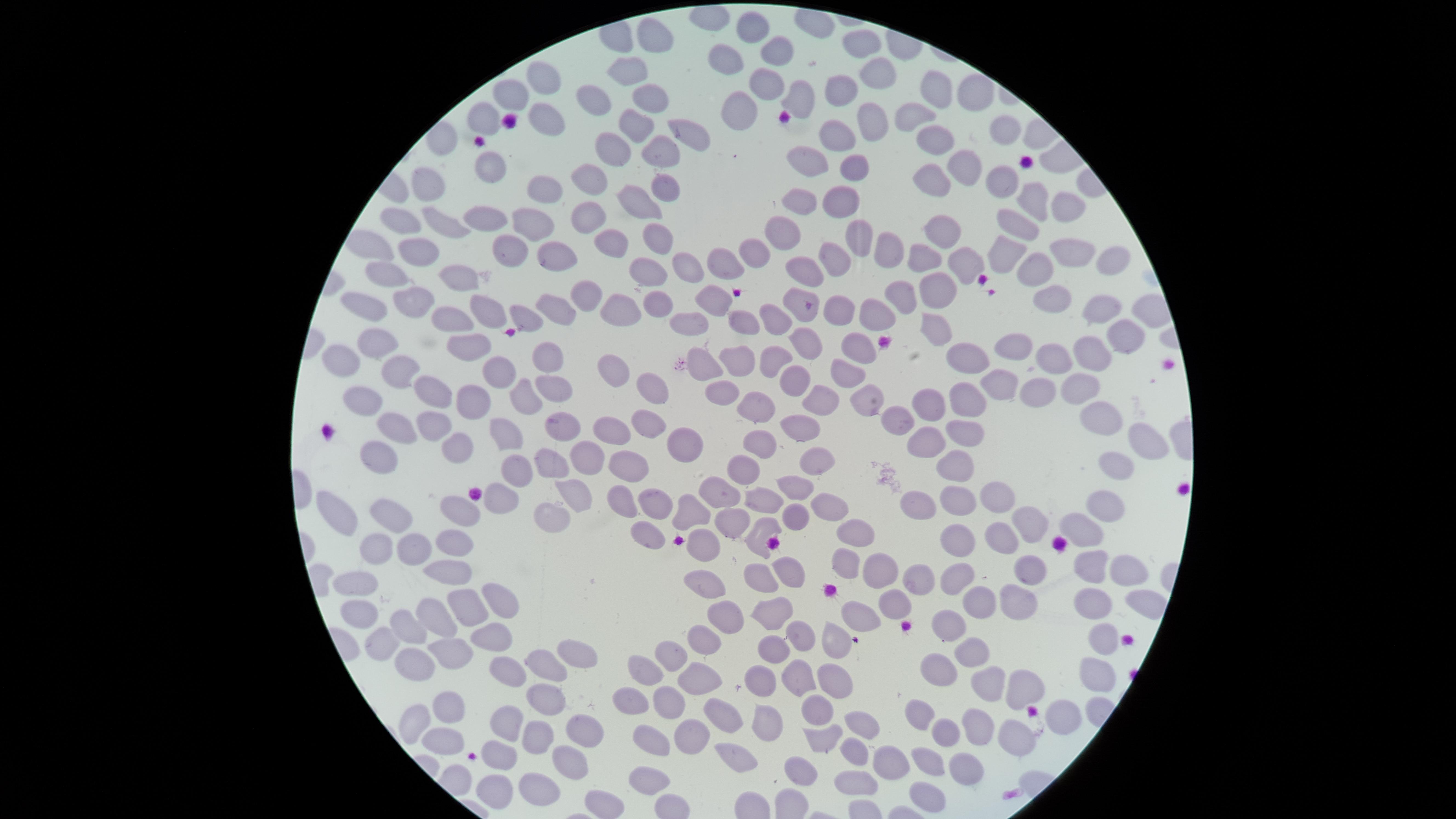

{
  "presence": "no malaria parasites detected",
  "preparation": "thin blood smear",
  "image_size": "1456×819 pixels",
  "capture": "smartphone photograph through the microscope eyepiece",
  "visible_region": "circular",
  "stain": "Giemsa",
  "field_of_view": "single",
  "uninfected_red_blood_cells": "approximate marker points as (x, y) in pixels: (753, 28), (651, 37), (862, 42), (770, 50), (722, 57), (632, 66), (875, 74), (543, 75), (764, 85), (834, 88), (511, 90), (937, 90), (971, 91), (647, 93), (591, 96), (799, 96), (737, 110), (914, 112), (485, 114), (547, 115), (872, 122), (631, 124), (688, 128), (1001, 130), (833, 136), (930, 136), (664, 152), (614, 154), (970, 161), (805, 162), (854, 165), (488, 166), (587, 172), (930, 177), (1003, 178), (430, 179), (540, 188), (659, 195), (803, 195), (1029, 197), (839, 198), (1065, 206), (635, 211), (485, 217), (587, 217), (401, 221), (531, 222), (446, 225), (1016, 225), (783, 226), (855, 237), (942, 237), (615, 239), (651, 239), (374, 241), (885, 246), (758, 247), (414, 249), (512, 249), (1072, 249), (1001, 251), (833, 255), (925, 257), (719, 259), (956, 260), (1108, 261), (555, 263), (686, 265), (648, 267), (808, 269), (389, 271), (1030, 271), (456, 273), (936, 283), (589, 290), (900, 294), (793, 297), (716, 298), (406, 300), (656, 303), (1052, 303), (366, 307), (838, 308), (551, 309), (620, 310), (1104, 310), (485, 314), (776, 314), (871, 314), (524, 316), (447, 320), (689, 320), (742, 320), (935, 324), (1127, 338), (374, 340), (808, 344), (1012, 346), (460, 347), (857, 351), (543, 352), (1089, 352), (968, 354), (1049, 354), (339, 356), (779, 356), (734, 359), (394, 362), (498, 368), (706, 368), (614, 371), (841, 375), (999, 381), (793, 382), (1076, 383), (549, 384), (435, 388), (1044, 388), (721, 389), (648, 391), (525, 392), (966, 398), (358, 400), (470, 402), (822, 402), (870, 402), (926, 402), (753, 406), (1096, 410), (430, 416), (897, 418), (648, 420), (391, 423), (561, 423), (801, 426), (502, 427), (606, 428), (969, 432), (685, 440), (928, 440), (758, 442), (452, 444), (1145, 447), (377, 455), (584, 456), (817, 460), (548, 465), (954, 465), (1115, 465), (622, 466), (516, 467), (746, 467), (796, 486), (719, 489), (574, 490), (999, 494), (767, 496), (621, 498), (496, 502), (917, 502), (652, 504), (948, 504), (823, 506), (1104, 509), (334, 511), (394, 511), (458, 512), (791, 515), (549, 516), (689, 517), (730, 522), (1033, 522), (1078, 524), (851, 531), (647, 532), (757, 534), (999, 535), (460, 538), (966, 538), (707, 545), (403, 547), (366, 548), (842, 559), (1086, 566), (451, 567), (787, 567), (1128, 571), (876, 572), (1024, 573), (965, 575), (918, 578), (762, 579), (355, 582), (707, 588), (492, 596), (1012, 599), (1090, 602), (893, 604), (973, 604), (1141, 605), (361, 606), (467, 607), (769, 611), (731, 614), (860, 617), (429, 620), (406, 625), (951, 625), (803, 636), (374, 639), (487, 639), (840, 642), (1105, 643), (698, 645), (449, 648), (768, 651), (972, 651), (674, 652), (575, 657), (416, 663), (542, 666), (511, 667), (938, 670), (799, 672), (641, 675), (832, 677), (695, 678), (1086, 678), (757, 682), (981, 685), (1024, 689), (548, 698), (632, 701), (670, 703), (452, 704), (814, 709), (913, 710), (1050, 715), (721, 716), (502, 721), (416, 722), (858, 722), (767, 724), (974, 727), (1013, 730), (944, 731), (575, 732), (685, 735), (537, 739), (819, 740), (443, 741), (655, 745), (893, 750), (737, 753), (853, 755), (500, 757), (924, 757), (564, 765), (958, 768), (800, 776), (646, 782), (854, 782), (536, 787), (492, 789), (924, 796), (601, 803)"
}